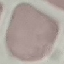
malaria_status: uninfected
capture: smartphone through the microscope eyepiece
image_type: cell patch, automatically extracted from a larger field of view and resized to 64 × 64 pixels
preparation: thin blood smear
stain: Giemsa